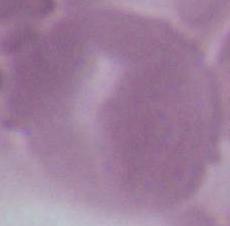
1000x magnification. An erythrocyte is seen. Micrograph.